Name the cell type shown.
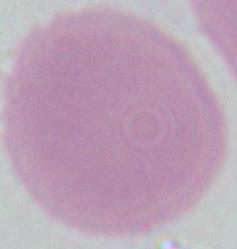

An erythrocyte.

{
  "modality": "photomicrograph",
  "magnification": "1000x"
}